Assess the morphology of the red blood cells.
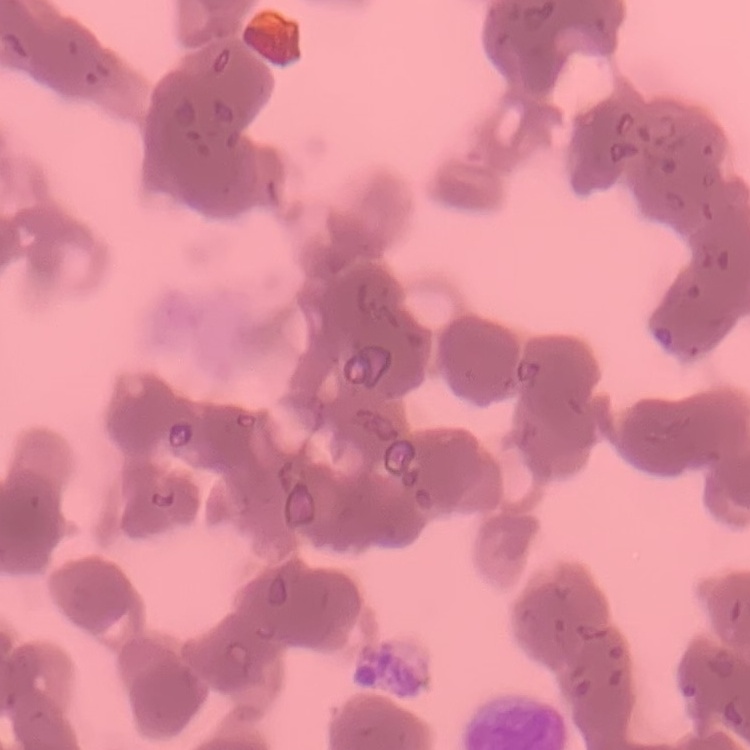

Rouleaux formation.

stain = Field's or Giemsa
preparation = thin peripheral smear
image type = square crop of a larger photomicrograph